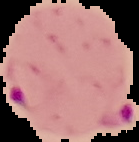
{
  "result": "malaria parasites detected",
  "image_type": "segmented cell region with the area outside set to black",
  "image_size": "139×142 pixels",
  "preparation": "thin blood film"
}